State the preparation type.
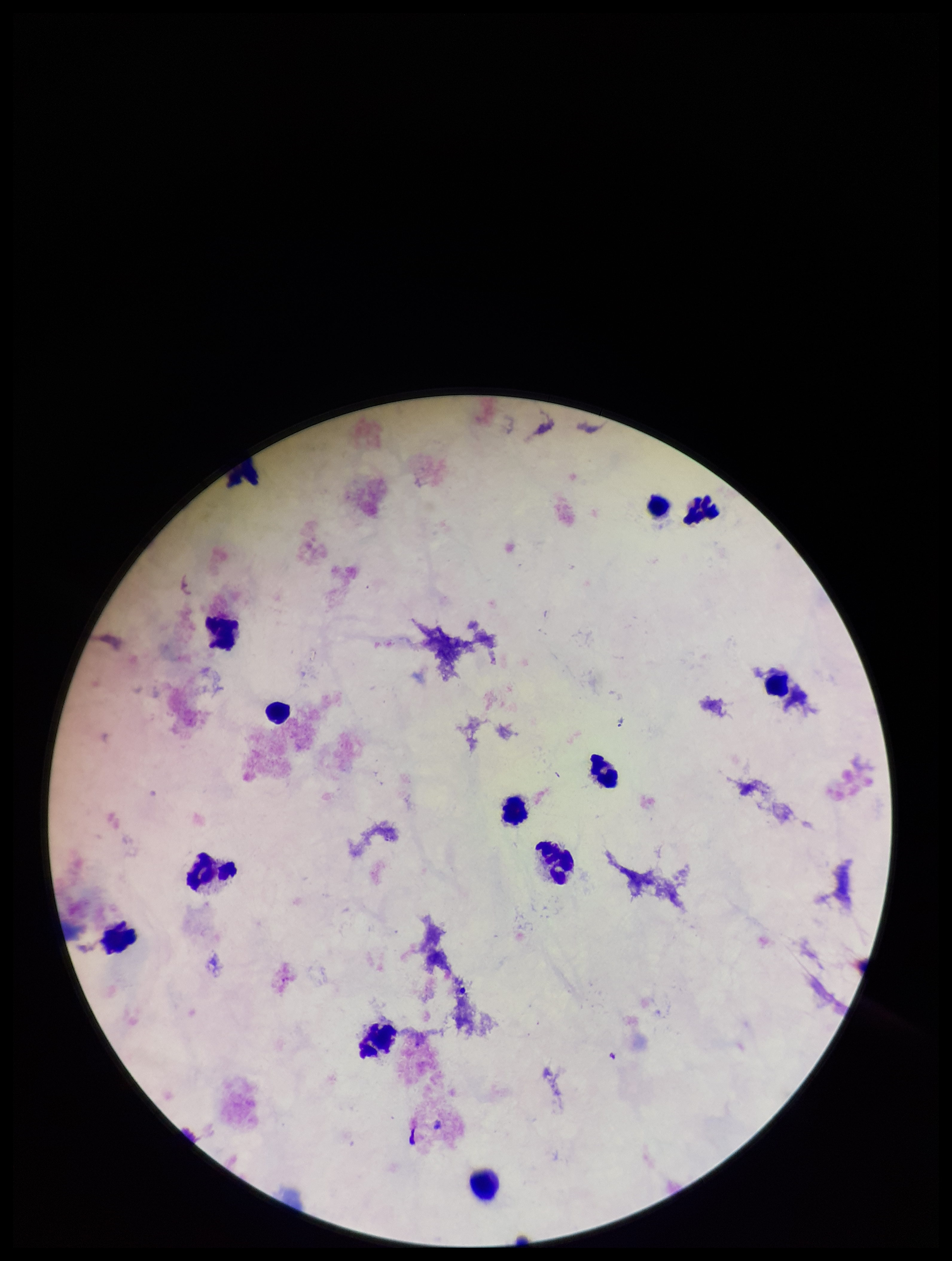

It is a thick blood smear.

image size = 952×1261 pixels
stain = Giemsa
Plasmodium parasites = none detected
leukocyte count = 13
capture = smartphone photograph through the microscope eyepiece
patient malaria status = negative
field of view = single
parasite count = 0